Report the malaria status of this cell.
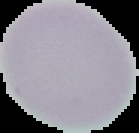

Uninfected.

Summary:
  - Preparation: thin blood film
  - Image type: segmented cell region with the area outside set to black
  - Image size: 139×133 pixels